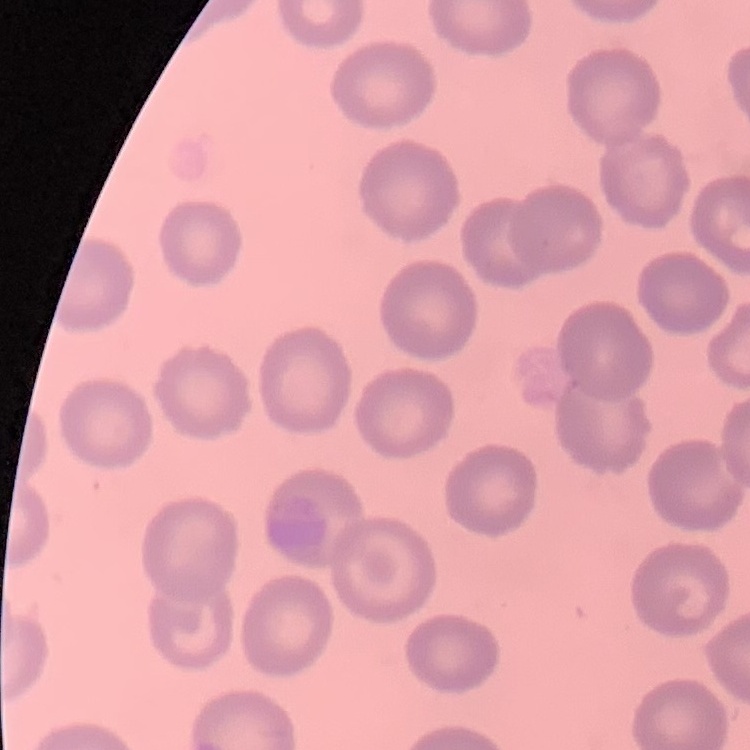

Summary:
  - Red blood cell morphology: no rouleaux formation
  - Preparation: thin peripheral smear
  - Image type: one tile cut from a larger photomicrograph
  - Stain: Field's or Giemsa